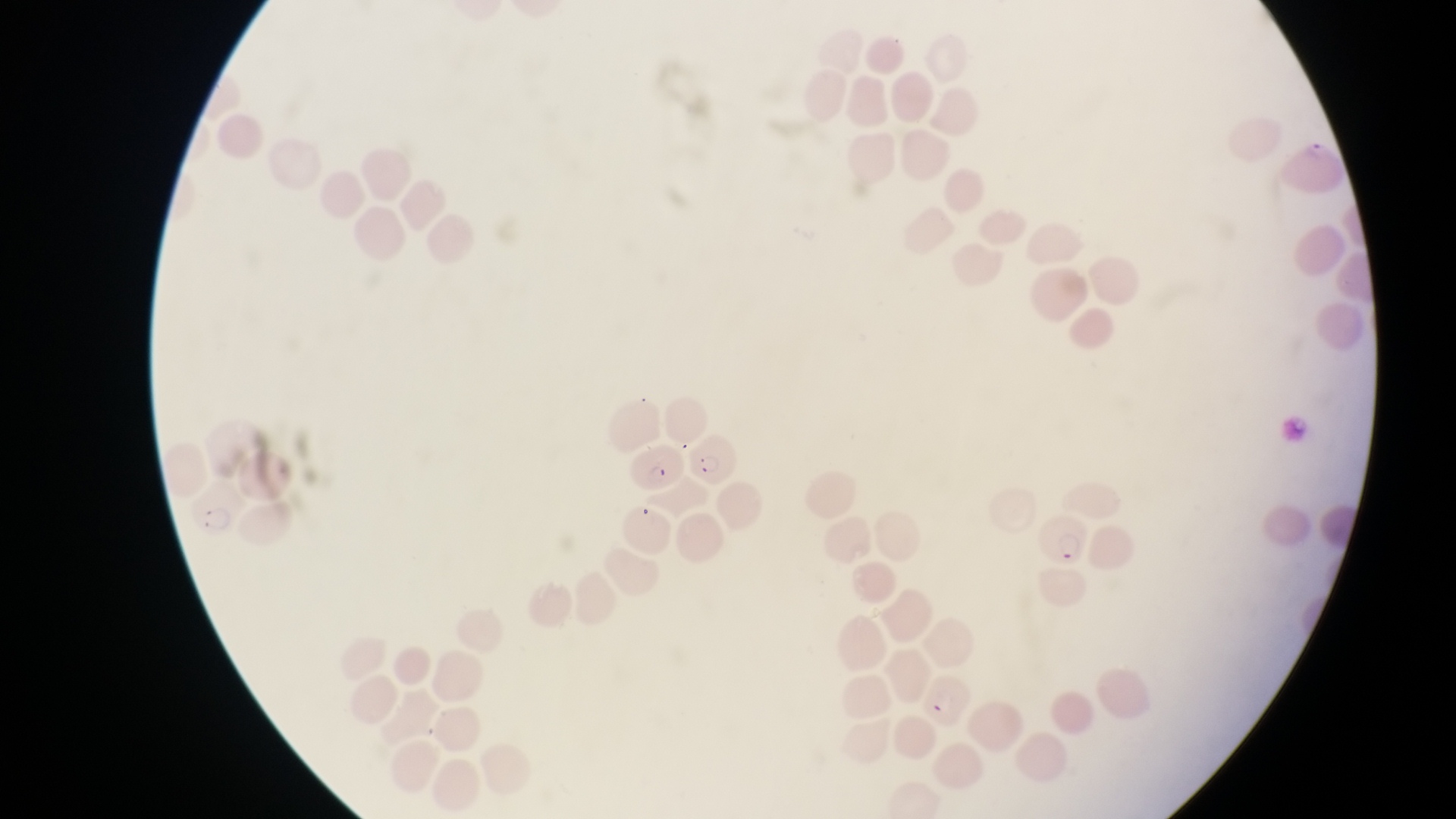

country = Uganda
image size = 1456×819 pixels
capture = smartphone photograph through the eyepiece of an Olympus CX-23 microscope
magnification = 1000x
preparation = thin blood film
field of view = single
parasitised red blood cell locations = approximate bounding boxes as (left, top, right, bottom) in pixels: (629, 438, 688, 497), (695, 438, 740, 488), (184, 479, 242, 542), (1041, 516, 1093, 572)